Identify the blood parasite species.
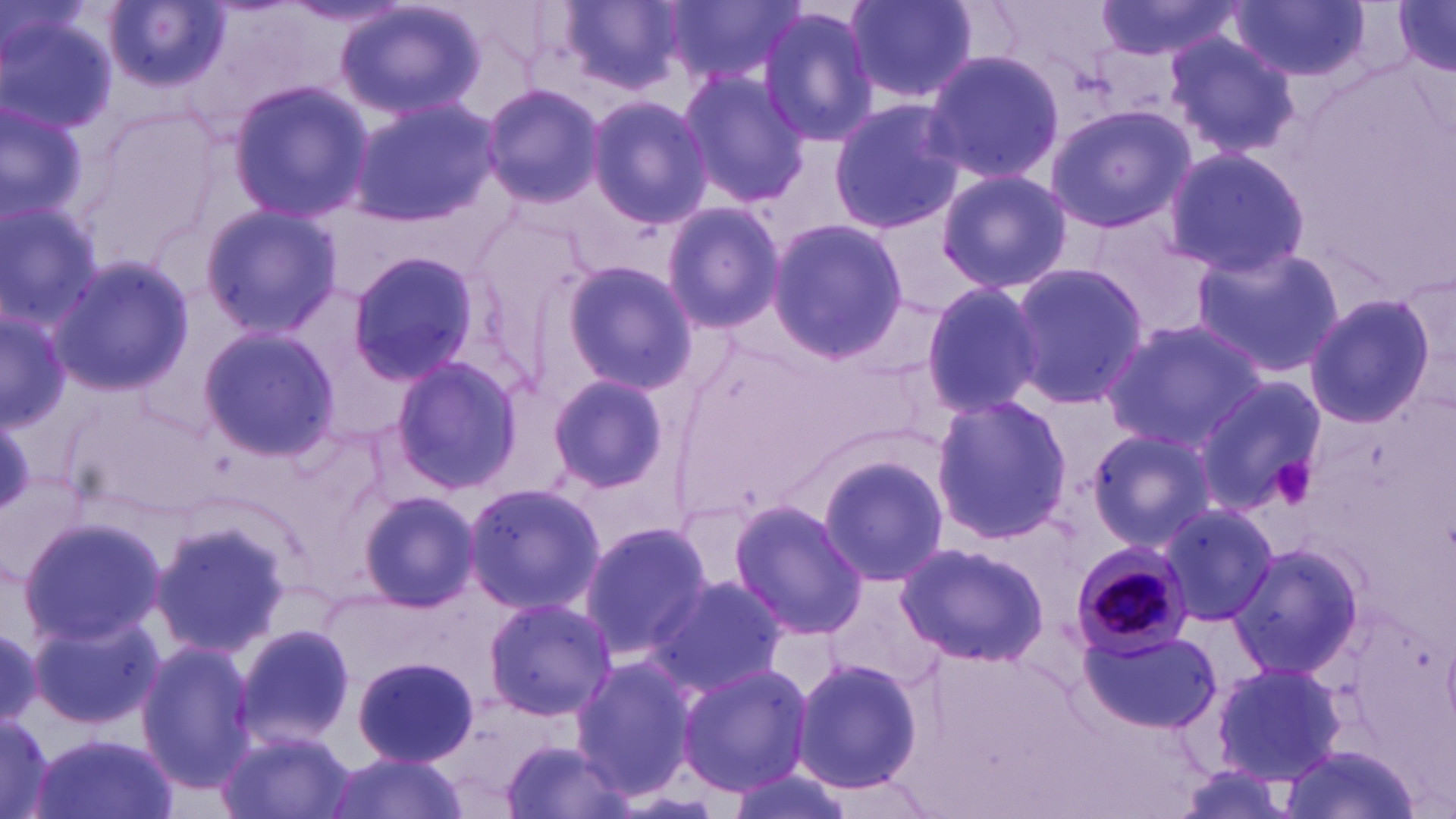
Plasmodium malariae.

Approximate bounding boxes as named x1/y1/x2/y2 corners in pixels. Plasmodium malariae-infected red blood cell locations: (x1=1067, y1=539, x2=1196, y2=658). Platelet locations: (x1=1269, y1=455, x2=1318, y2=508). Uninfected red blood cell locations: (x1=333, y1=0, x2=487, y2=122), (x1=841, y1=0, x2=981, y2=105), (x1=1093, y1=0, x2=1250, y2=63), (x1=1229, y1=0, x2=1370, y2=82), (x1=1390, y1=0, x2=1456, y2=77), (x1=555, y1=1, x2=686, y2=96), (x1=665, y1=1, x2=805, y2=87), (x1=106, y1=2, x2=228, y2=95), (x1=1, y1=4, x2=118, y2=140), (x1=756, y1=7, x2=881, y2=146), (x1=1162, y1=30, x2=1299, y2=159), (x1=921, y1=51, x2=1065, y2=183), (x1=676, y1=68, x2=809, y2=207), (x1=228, y1=81, x2=373, y2=220), (x1=479, y1=84, x2=603, y2=208), (x1=584, y1=94, x2=711, y2=231), (x1=827, y1=98, x2=964, y2=235), (x1=348, y1=99, x2=496, y2=225), (x1=0, y1=103, x2=90, y2=222), (x1=1044, y1=106, x2=1192, y2=234), (x1=1163, y1=146, x2=1311, y2=279), (x1=937, y1=167, x2=1071, y2=295), (x1=0, y1=198, x2=104, y2=334), (x1=660, y1=200, x2=783, y2=335), (x1=200, y1=205, x2=341, y2=336), (x1=765, y1=219, x2=910, y2=362), (x1=1189, y1=246, x2=1343, y2=378), (x1=348, y1=251, x2=480, y2=386), (x1=48, y1=254, x2=195, y2=397), (x1=557, y1=260, x2=698, y2=393), (x1=1008, y1=261, x2=1146, y2=409), (x1=917, y1=279, x2=1046, y2=419), (x1=1302, y1=294, x2=1437, y2=429), (x1=2, y1=308, x2=69, y2=430), (x1=1101, y1=319, x2=1265, y2=454), (x1=196, y1=326, x2=339, y2=462), (x1=388, y1=355, x2=522, y2=496), (x1=543, y1=371, x2=671, y2=495), (x1=1193, y1=376, x2=1327, y2=517), (x1=930, y1=396, x2=1070, y2=544), (x1=1086, y1=427, x2=1220, y2=552), (x1=815, y1=452, x2=949, y2=587), (x1=463, y1=479, x2=607, y2=615), (x1=359, y1=490, x2=480, y2=610), (x1=727, y1=498, x2=867, y2=640), (x1=1156, y1=501, x2=1278, y2=627), (x1=17, y1=514, x2=166, y2=649), (x1=579, y1=517, x2=713, y2=660), (x1=151, y1=519, x2=293, y2=656), (x1=894, y1=538, x2=1048, y2=669), (x1=1231, y1=539, x2=1367, y2=678), (x1=649, y1=575, x2=789, y2=698), (x1=826, y1=579, x2=946, y2=687), (x1=481, y1=595, x2=617, y2=721), (x1=31, y1=614, x2=163, y2=732), (x1=235, y1=624, x2=358, y2=750), (x1=1081, y1=627, x2=1221, y2=736), (x1=136, y1=641, x2=259, y2=792), (x1=791, y1=656, x2=924, y2=796), (x1=572, y1=657, x2=699, y2=795), (x1=353, y1=658, x2=478, y2=767), (x1=1210, y1=659, x2=1347, y2=785), (x1=675, y1=661, x2=812, y2=795), (x1=0, y1=711, x2=54, y2=819), (x1=218, y1=728, x2=352, y2=819), (x1=29, y1=733, x2=178, y2=819), (x1=502, y1=735, x2=633, y2=819), (x1=1281, y1=747, x2=1423, y2=819), (x1=319, y1=751, x2=474, y2=819), (x1=720, y1=761, x2=853, y2=819). Light microscopy. Image is 1456×819 pixels. Single field of view. Thin blood film. 1000x magnification. May-Grünwald-Giemsa stain.